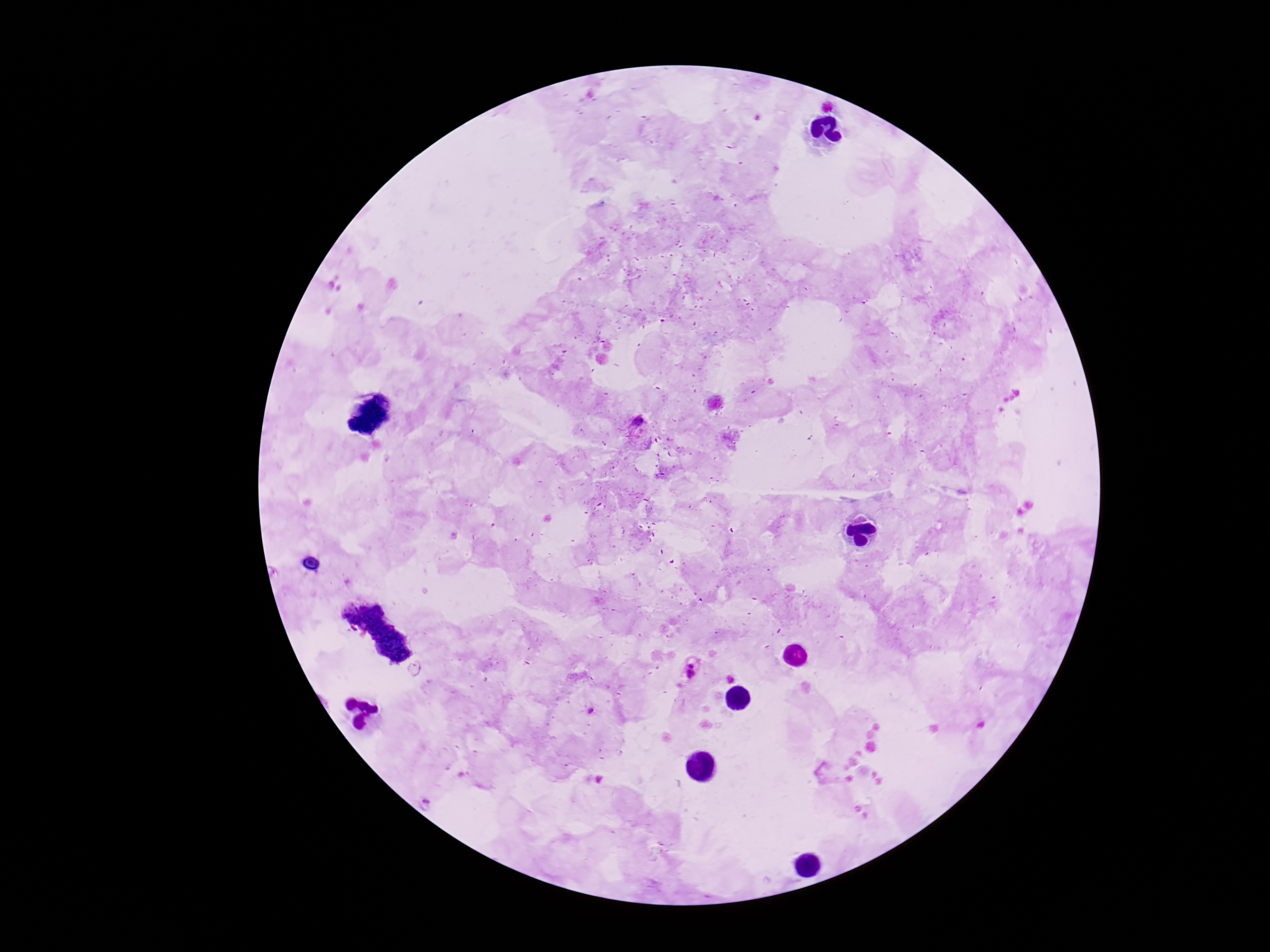 Approximate object centers, in pixels from the top-left corner. Plasmodium parasite locations: (x=826, y=104), (x=641, y=430), (x=691, y=672). Image is 1270×952 pixels. Single field of view. Giemsa stain. Thick blood film. Patient malaria status: positive. Smartphone photograph taken through the microscope eyepiece. 100x magnification.